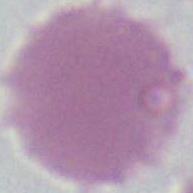
Photomicrograph. An erythrocyte is shown. 1000x magnification.